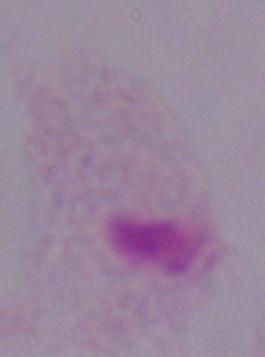

A trichomonad is seen. Micrograph. Captured at 1000x magnification.